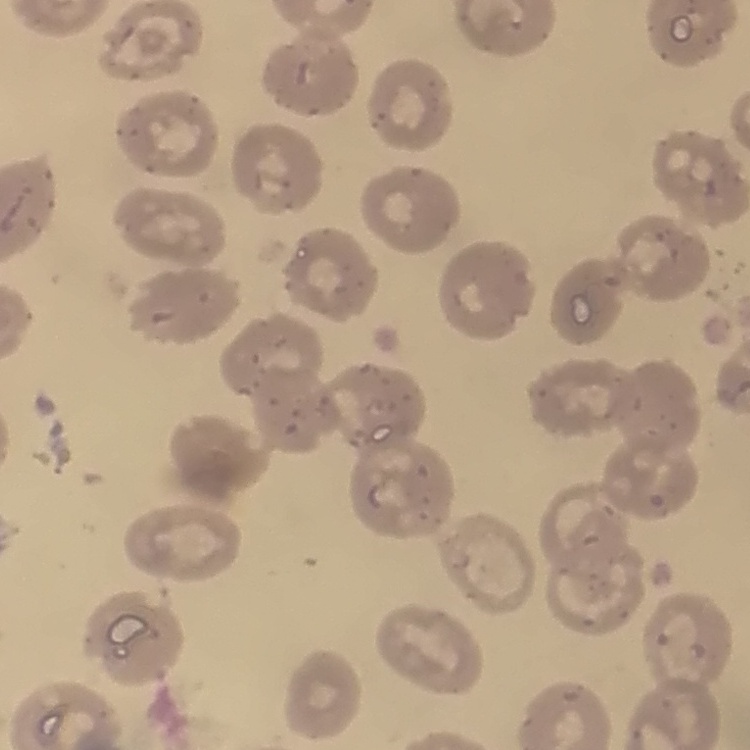 The erythrocytes exhibit no rouleaux formation. Stained with either Field's or Giemsa. Thin blood film. One tile cut from a larger photomicrograph.